Outline each Plasmodium malariae-infected red blood cell.
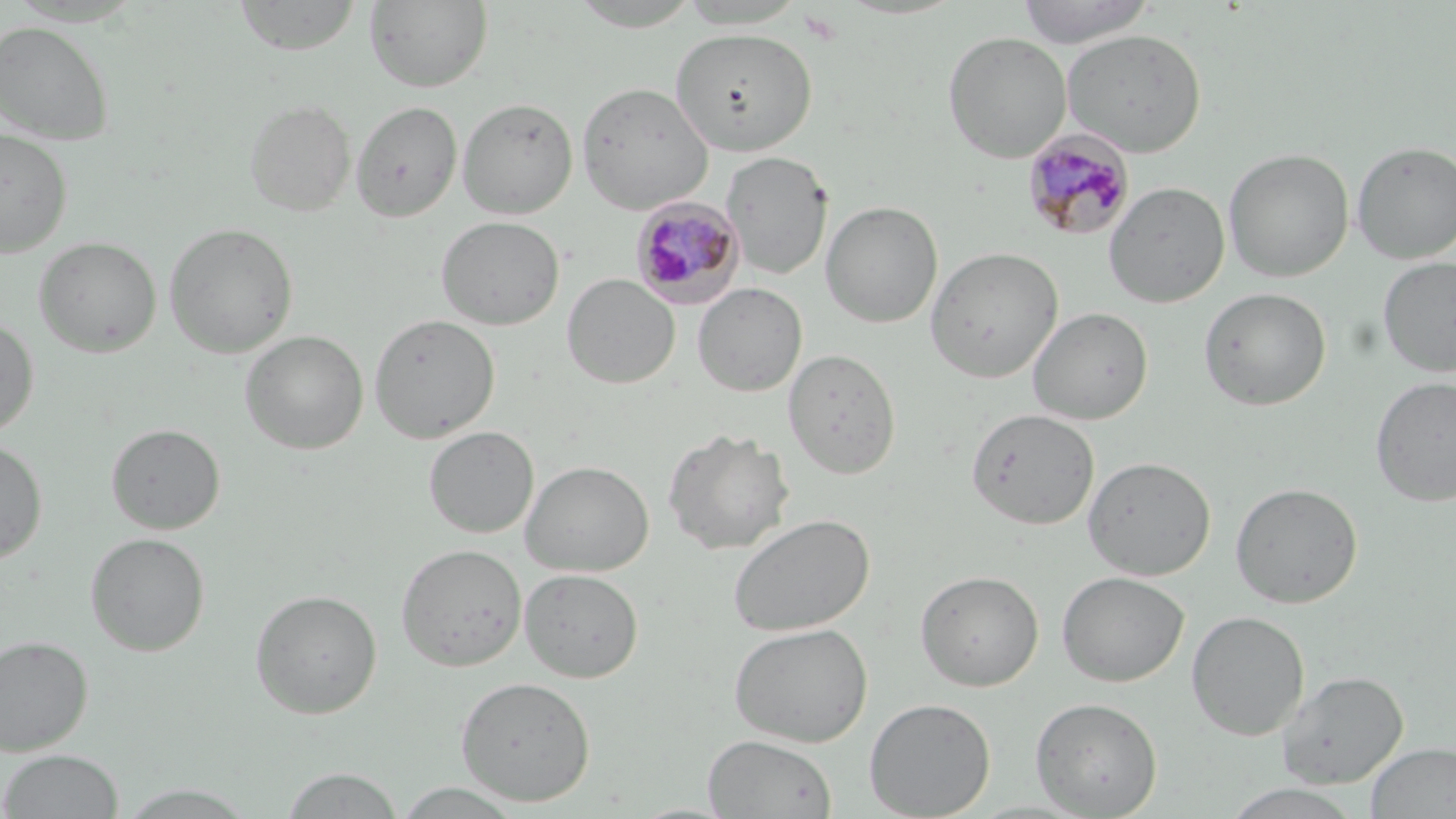
Approximate bounding boxes as (x1, y1, x2, y2) in pixels.
Plasmodium malariae-infected red blood cells: (1023, 129, 1135, 242), (630, 196, 745, 308).

Summary:
  - Uninfected red blood cell locations: (232, 0, 363, 56), (365, 0, 492, 92), (1015, 0, 1156, 47), (565, 1, 707, 31), (0, 20, 115, 145), (670, 26, 817, 155), (1062, 28, 1206, 156), (943, 31, 1072, 163), (576, 81, 713, 214), (457, 97, 578, 218), (243, 98, 356, 217), (351, 100, 462, 221), (0, 128, 72, 257), (1351, 140, 1456, 263), (1223, 148, 1354, 282), (721, 150, 833, 280), (1104, 181, 1230, 308), (821, 200, 943, 328), (436, 216, 564, 330), (164, 222, 298, 358), (33, 236, 162, 357), (925, 246, 1063, 383), (1378, 257, 1456, 378), (562, 273, 680, 389), (692, 283, 807, 397), (1199, 287, 1331, 410), (1027, 306, 1153, 424), (368, 313, 500, 443), (0, 317, 39, 438), (240, 330, 369, 455), (783, 349, 901, 479), (1370, 375, 1456, 506), (966, 407, 1100, 530), (105, 423, 226, 534), (424, 426, 539, 538), (663, 428, 795, 555), (0, 440, 48, 564), (1083, 456, 1216, 580), (520, 460, 654, 576), (1230, 481, 1363, 608), (728, 514, 874, 637), (85, 532, 211, 656), (396, 543, 527, 671), (519, 568, 644, 683), (915, 569, 1044, 691), (1057, 571, 1189, 687), (249, 588, 382, 719), (1187, 610, 1310, 740), (729, 623, 873, 746), (0, 635, 93, 755), (1277, 670, 1408, 787), (455, 676, 596, 806), (1030, 696, 1163, 817), (864, 698, 996, 819), (703, 734, 838, 818), (1365, 742, 1456, 818), (0, 749, 124, 818), (280, 767, 404, 818), (392, 782, 526, 818), (1220, 783, 1365, 819), (117, 784, 256, 818)
  - Slide-level diagnosis: Plasmodium malariae
  - Stain: May-Grünwald-Giemsa
  - Field of view: one of a larger specimen
  - Modality: light microscopy
  - Magnification: 1000x
  - Preparation: thin blood film
  - Image size: 1456×819 pixels